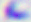

{
  "modality": "photomicrograph",
  "magnification": "400x",
  "identification": "Toxoplasma gondii"
}